Report the malaria status of this cell.
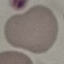

It is uninfected.

Summary:
  - Capture: smartphone camera at the microscope eyepiece
  - Stain: Giemsa
  - Image type: cell patch, automatically extracted from a larger field of view and resized to 64 × 64 pixels
  - Preparation: thin blood film